Assess this cell for malaria.
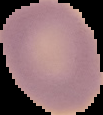
It is uninfected.

Summary:
  - Image size: 103×115 pixels
  - Image type: cell region segmented out of the field of view; surrounding area masked to black
  - Preparation: thin blood smear